Outline each Plasmodium parasite.
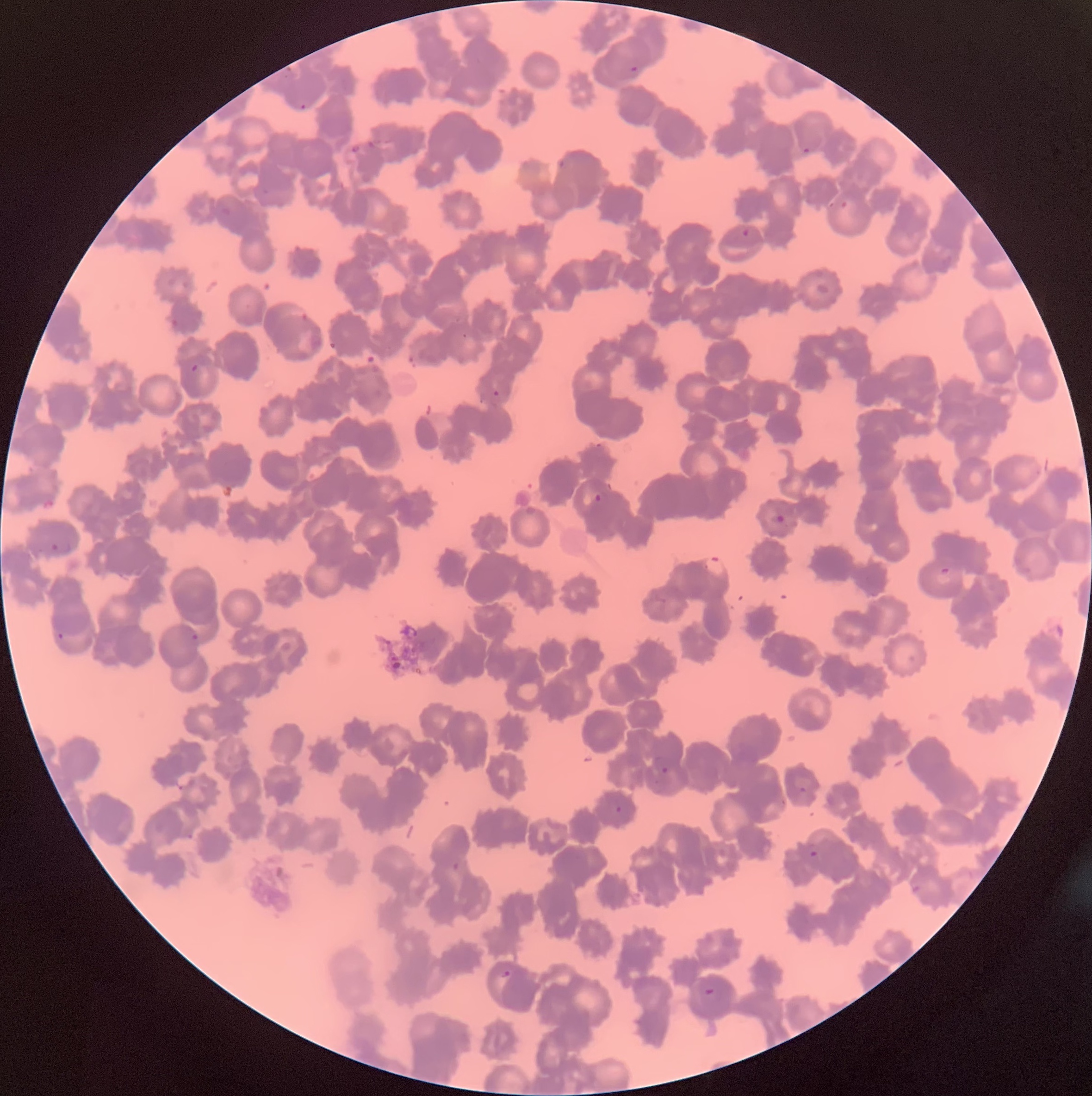

Approximate bounding boxes as (x1,y1)-(x2,y2) corner pairs in pixels.
Plasmodium parasites: (629,64)-(638,73), (300,103)-(308,112), (350,143)-(361,154), (802,145)-(810,155), (741,227)-(749,237), (191,363)-(200,373), (493,390)-(500,398), (593,492)-(603,503), (775,514)-(785,523), (50,541)-(72,556), (702,555)-(727,579), (939,566)-(951,576), (57,632)-(64,640), (190,632)-(200,642), (660,766)-(670,775), (797,785)-(807,794), (615,805)-(623,813), (809,850)-(819,859), (501,969)-(512,978), (704,987)-(715,996).
Plasmodium parasites too small for a box (approximate centers as (x,y) in pixels): (464,335).

Image is 1092×1096 pixels. The red blood cells show rouleaux formation. Light microscopy. Thin blood smear.